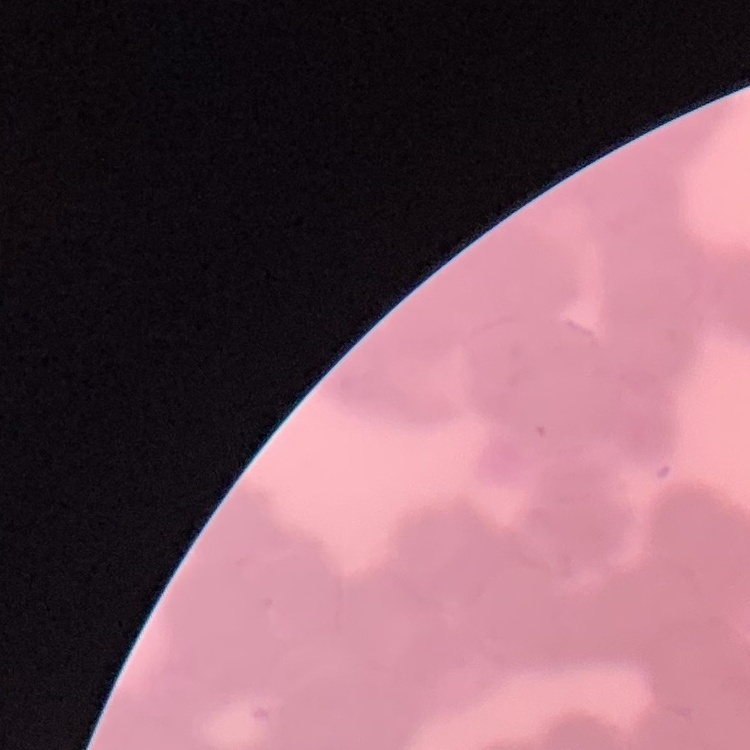

red blood cell morphology = rouleaux formation
stain = Field's or Giemsa
image type = square crop of a larger photomicrograph
preparation = thin peripheral smear